Locate every blood parasite and identify its species.
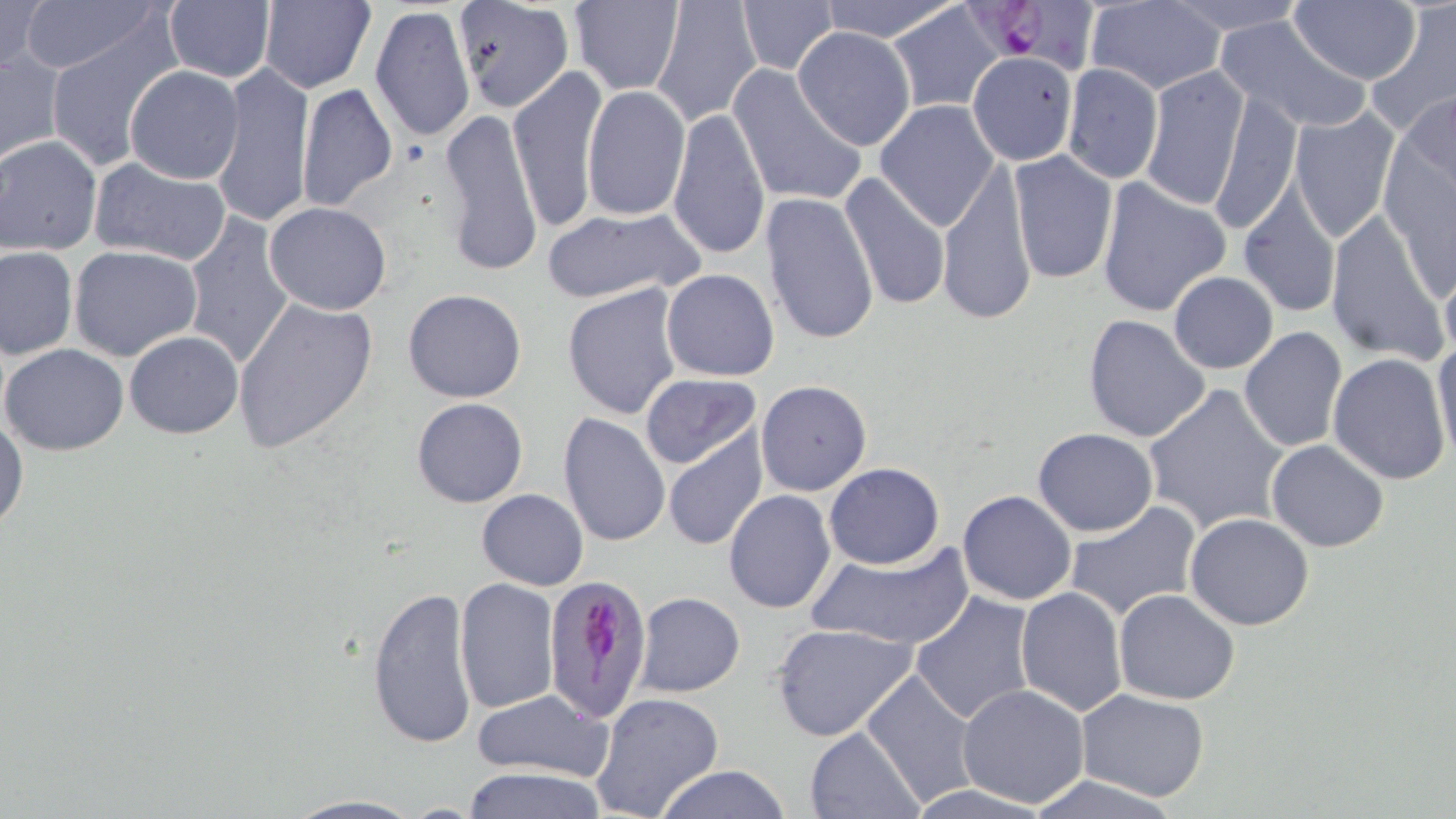
Approximate bounding boxes as (x1,y1)-(x2,y2) corner pairs in pixels.
Plasmodium falciparum-infected red blood cells: (964,0)-(1106,79), (542,577)-(651,724).
No Plasmodium ovale, Plasmodium malariae, Plasmodium vivax, Babesia divergens, or Trypanosoma brucei observed.

Uninfected red blood cell locations: (18,0)-(163,73), (258,0)-(375,93), (452,0)-(575,114), (569,0)-(684,95), (650,0)-(763,127), (816,0)-(963,42), (1084,0)-(1227,94), (1160,0)-(1312,34), (1289,0)-(1421,86), (0,1)-(47,80), (163,1)-(277,84), (735,1)-(838,77), (883,3)-(1006,113), (370,4)-(476,147), (1364,4)-(1456,140), (1215,14)-(1371,134), (44,24)-(185,169), (791,27)-(916,150), (1,48)-(65,162), (969,57)-(1086,173), (213,62)-(314,228), (1062,63)-(1163,182), (728,64)-(868,209), (1137,65)-(1251,213), (124,66)-(244,184), (507,66)-(607,233), (296,82)-(398,214), (582,86)-(690,221), (1207,91)-(1301,236), (1399,91)-(1456,201), (875,100)-(999,230), (439,106)-(544,277), (666,107)-(770,263), (1287,107)-(1399,243), (1215,120)-(1318,299), (1,136)-(102,255), (1007,150)-(1118,284), (937,154)-(1039,330), (88,157)-(230,267), (838,171)-(951,312), (1096,178)-(1232,318), (1237,188)-(1341,319), (760,192)-(880,347), (263,202)-(393,316), (540,205)-(705,304), (1324,211)-(1448,362), (183,213)-(296,369), (0,245)-(77,359), (69,245)-(202,362), (1439,264)-(1456,365), (662,268)-(780,381), (1168,271)-(1278,374), (561,281)-(684,421), (403,288)-(528,403), (233,297)-(378,453), (1083,314)-(1211,443), (1238,327)-(1347,453), (123,331)-(244,439), (1431,335)-(1456,470), (1,343)-(129,455), (1328,352)-(1454,486), (640,373)-(762,471), (754,380)-(871,497), (1142,382)-(1289,535), (411,396)-(528,508), (0,412)-(29,535), (557,412)-(670,545), (1031,428)-(1159,537), (662,432)-(769,552), (1266,440)-(1391,552), (823,462)-(944,568), (476,488)-(588,590), (723,490)-(835,613), (956,491)-(1077,607), (1064,500)-(1205,624), (1185,513)-(1314,630), (806,542)-(974,651), (454,578)-(561,715), (367,582)-(478,750), (1015,587)-(1127,719), (1113,589)-(1240,706), (634,592)-(745,697), (910,592)-(1036,725), (770,623)-(916,741), (861,668)-(980,807), (957,685)-(1091,808), (1076,689)-(1209,802), (473,690)-(613,781), (590,692)-(725,819), (805,727)-(922,817), (650,764)-(791,819), (456,766)-(612,819), (1028,774)-(1183,819), (278,794)-(429,818). Slide-level diagnosis: Plasmodium falciparum. 1000x magnification. Thin blood smear. One field of a larger specimen. Optical microscopy. Image is 1456×819 pixels. May-Grünwald-Giemsa-stained preparation.